Assess for malaria.
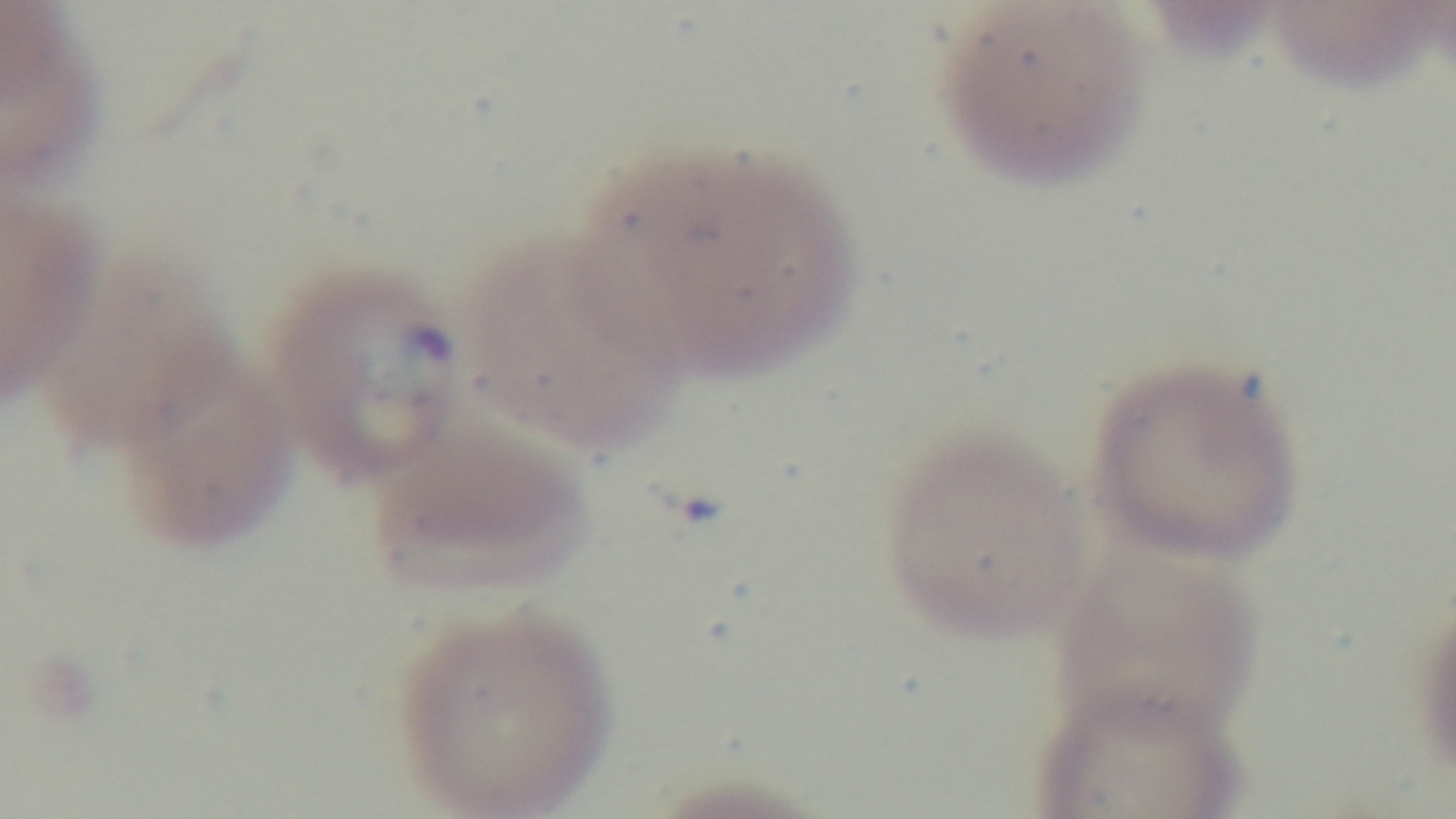

Infected.

Preparation: thin. Oil-immersion objective, 100x. Photomicrograph. Giemsa stain. One field from the slide. Mounted 4K digital camera.